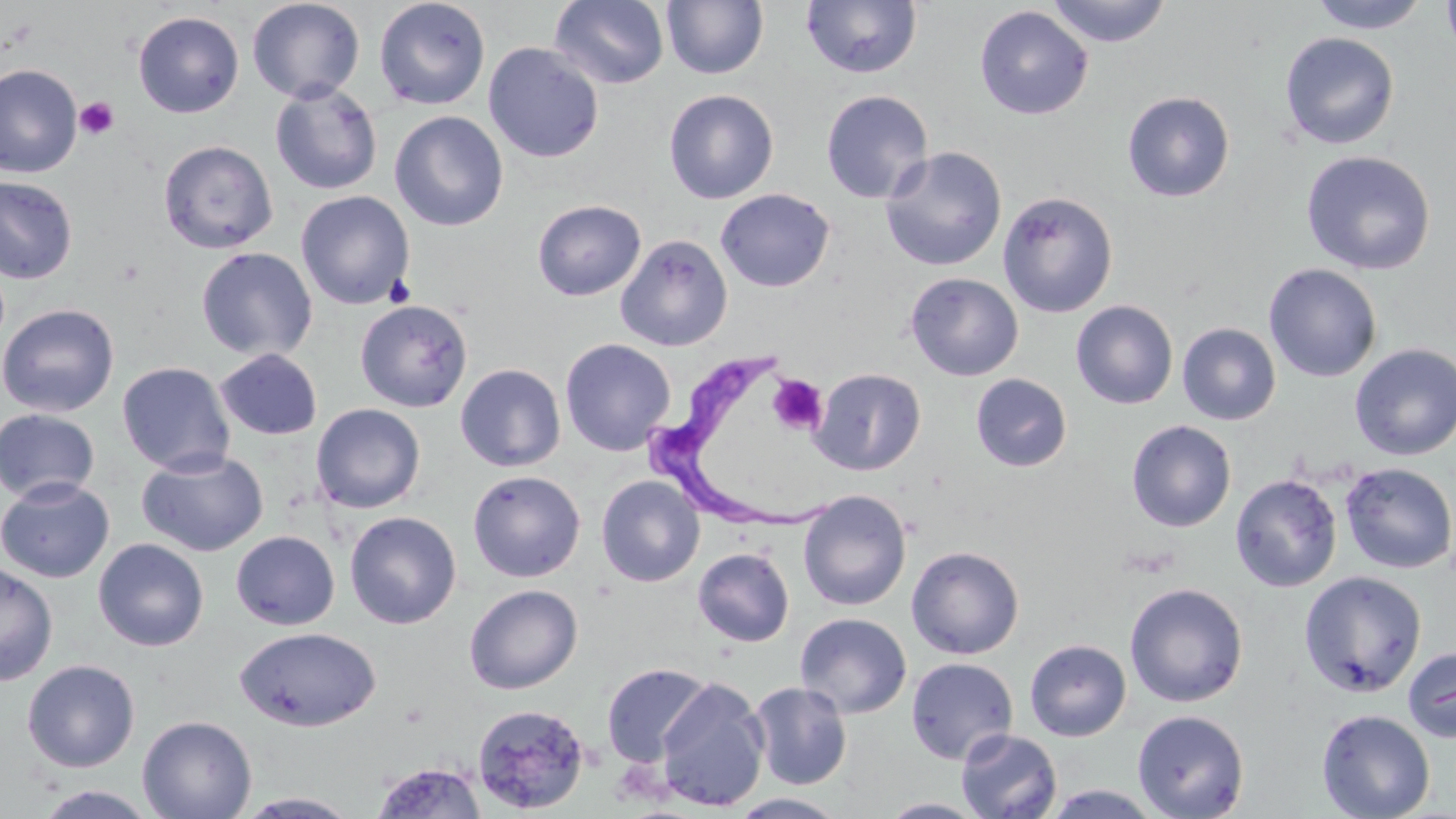
Summary:
  - Coordinate format: approximate bounding boxes as (x1, y1, x2, y2) in pixels
  - Platelet locations: (74, 97, 119, 141), (768, 374, 828, 435)
  - Uninfected red blood cell locations: (247, 0, 365, 104), (373, 0, 491, 110), (1047, 0, 1170, 47), (1309, 0, 1429, 33), (1441, 0, 1456, 58), (550, 1, 670, 89), (662, 1, 768, 80), (801, 1, 922, 79), (974, 6, 1093, 120), (132, 11, 245, 118), (1280, 32, 1399, 150), (483, 42, 604, 163), (0, 64, 83, 178), (269, 81, 383, 195), (663, 89, 779, 204), (821, 90, 934, 204), (1121, 91, 1235, 202), (389, 110, 509, 232), (157, 139, 279, 254), (880, 146, 1007, 271), (1300, 150, 1436, 275), (0, 175, 79, 285), (715, 188, 835, 292), (296, 190, 415, 310), (997, 191, 1119, 318), (531, 199, 646, 301), (615, 233, 733, 352), (195, 246, 318, 362), (1263, 262, 1382, 383), (904, 272, 1024, 381), (354, 299, 473, 413), (1071, 300, 1178, 410), (0, 302, 120, 418), (1177, 323, 1281, 426), (559, 338, 676, 456), (1350, 343, 1456, 461), (214, 348, 323, 441), (116, 361, 236, 476), (455, 363, 566, 472), (811, 368, 926, 476), (970, 373, 1072, 472), (310, 403, 427, 514), (0, 407, 101, 504), (1127, 420, 1236, 532), (136, 448, 268, 557), (1339, 462, 1456, 574), (467, 469, 586, 582), (1229, 473, 1343, 593), (596, 475, 705, 587), (0, 476, 116, 583), (798, 489, 911, 611), (344, 510, 462, 629), (231, 530, 340, 630), (92, 537, 209, 652), (906, 545, 1025, 660), (692, 547, 795, 647), (0, 560, 59, 687), (1299, 571, 1427, 697), (1124, 583, 1248, 708), (464, 584, 583, 694), (794, 612, 912, 718), (234, 625, 381, 731), (1024, 639, 1132, 741), (1402, 645, 1456, 743), (906, 657, 1019, 765), (22, 659, 140, 772), (600, 662, 714, 768), (653, 678, 769, 812), (748, 681, 853, 790), (471, 702, 592, 815), (1132, 709, 1250, 819), (1317, 709, 1436, 819), (137, 714, 257, 819), (956, 729, 1063, 818), (369, 761, 489, 818), (30, 785, 162, 819), (1041, 785, 1167, 818), (234, 791, 364, 818), (728, 793, 852, 818), (877, 797, 990, 818)
  - Trypanosoma brucei locations: (637, 356, 835, 528)
  - Slide-level diagnosis: Trypanosoma brucei
  - Preparation: thin blood film
  - Field of view: one of a larger specimen
  - Image size: 1456×819 pixels
  - Modality: optical microscopy
  - Stain: May-Grünwald-Giemsa
  - Magnification: 1000x